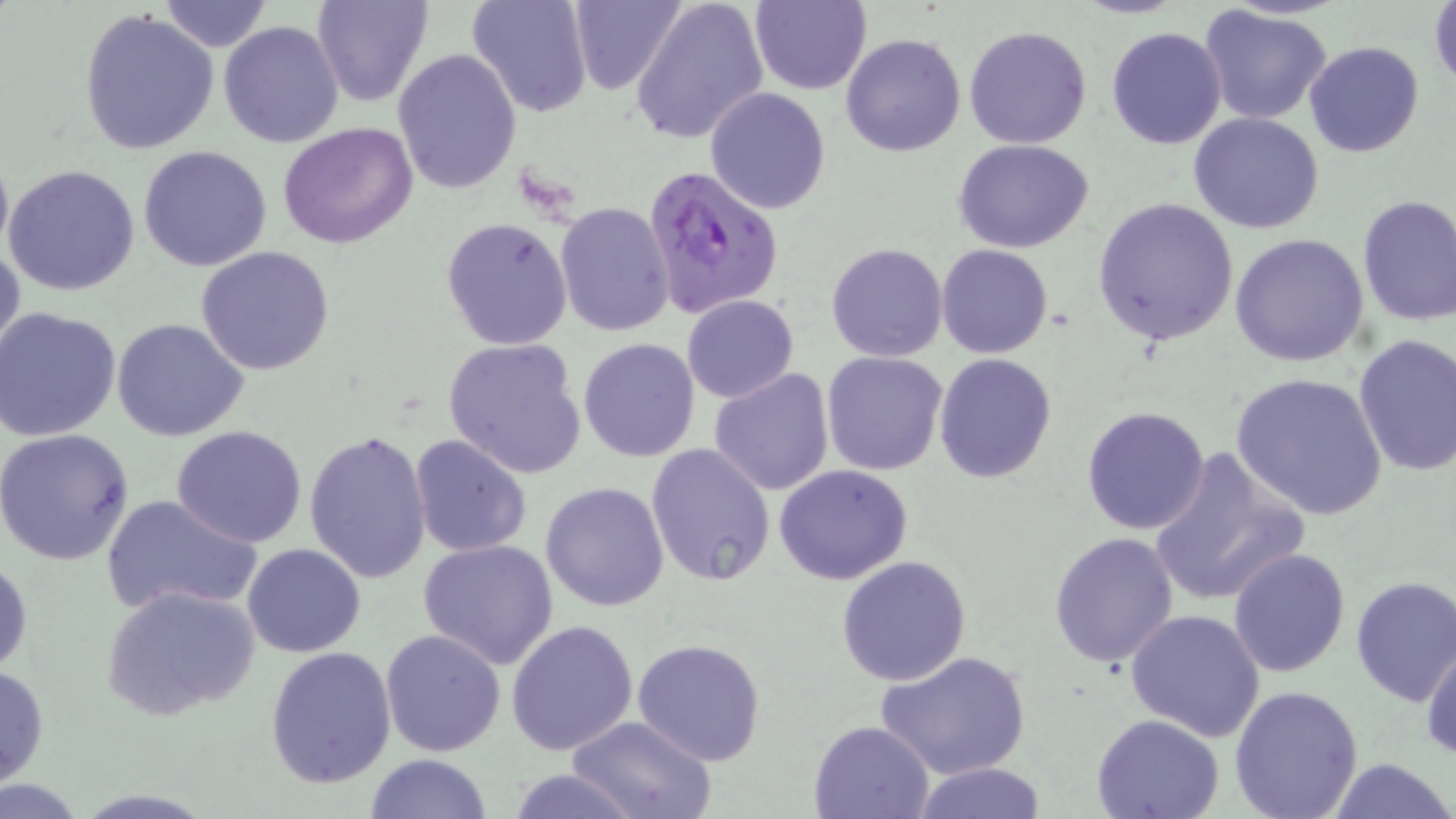

Summary:
  - Coordinate format: approximate bounding boxes as (x1, y1, x2, y2) in pixels
  - Plasmodium falciparum-infected red blood cell locations: (643, 164, 783, 320)
  - Uninfected red blood cell locations: (311, 0, 433, 107), (466, 0, 593, 119), (568, 0, 689, 95), (629, 0, 770, 146), (750, 0, 872, 96), (158, 1, 274, 51), (1428, 1, 1456, 93), (1199, 5, 1335, 127), (76, 10, 221, 155), (218, 20, 345, 149), (963, 25, 1093, 150), (1105, 26, 1228, 150), (841, 33, 966, 156), (1304, 40, 1425, 159), (392, 48, 521, 194), (704, 86, 832, 215), (1189, 112, 1325, 235), (278, 122, 420, 248), (954, 138, 1096, 253), (0, 141, 13, 273), (138, 145, 272, 272), (4, 163, 141, 295), (1356, 195, 1456, 326), (1094, 197, 1241, 345), (554, 201, 674, 338), (441, 216, 573, 351), (1228, 233, 1371, 367), (0, 238, 25, 369), (825, 242, 949, 363), (936, 244, 1054, 360), (195, 246, 335, 375), (681, 294, 798, 402), (1, 307, 123, 442), (112, 318, 251, 443), (1352, 334, 1456, 477), (441, 336, 589, 482), (578, 337, 702, 462), (821, 351, 949, 476), (934, 353, 1056, 483), (708, 368, 835, 497), (1231, 374, 1387, 519), (1082, 406, 1211, 536), (169, 425, 309, 548), (1, 426, 135, 565), (304, 430, 434, 587), (408, 434, 532, 558), (645, 442, 775, 586), (1147, 447, 1310, 609), (773, 464, 916, 585), (541, 480, 670, 612), (101, 491, 261, 618), (1049, 531, 1180, 669), (416, 538, 560, 668), (242, 542, 365, 657), (1227, 548, 1352, 679), (0, 554, 33, 678), (835, 555, 972, 687), (1350, 575, 1456, 707), (100, 584, 262, 725), (1125, 608, 1265, 742), (507, 621, 639, 755), (381, 628, 506, 755), (631, 637, 767, 768), (1420, 638, 1456, 764), (265, 645, 398, 789), (875, 650, 1032, 781), (0, 663, 49, 789), (1229, 684, 1363, 819), (568, 714, 715, 819), (1090, 714, 1225, 819), (807, 719, 935, 819), (362, 753, 495, 818), (1328, 757, 1454, 818), (907, 764, 1049, 818), (503, 768, 642, 819)
  - Slide-level diagnosis: Plasmodium falciparum
  - Preparation: thin blood film
  - Stain: May-Grünwald-Giemsa
  - Magnification: 1000x
  - Field of view: single
  - Modality: light microscopy
  - Image size: 1456×819 pixels